Point out every Plasmodium parasite.
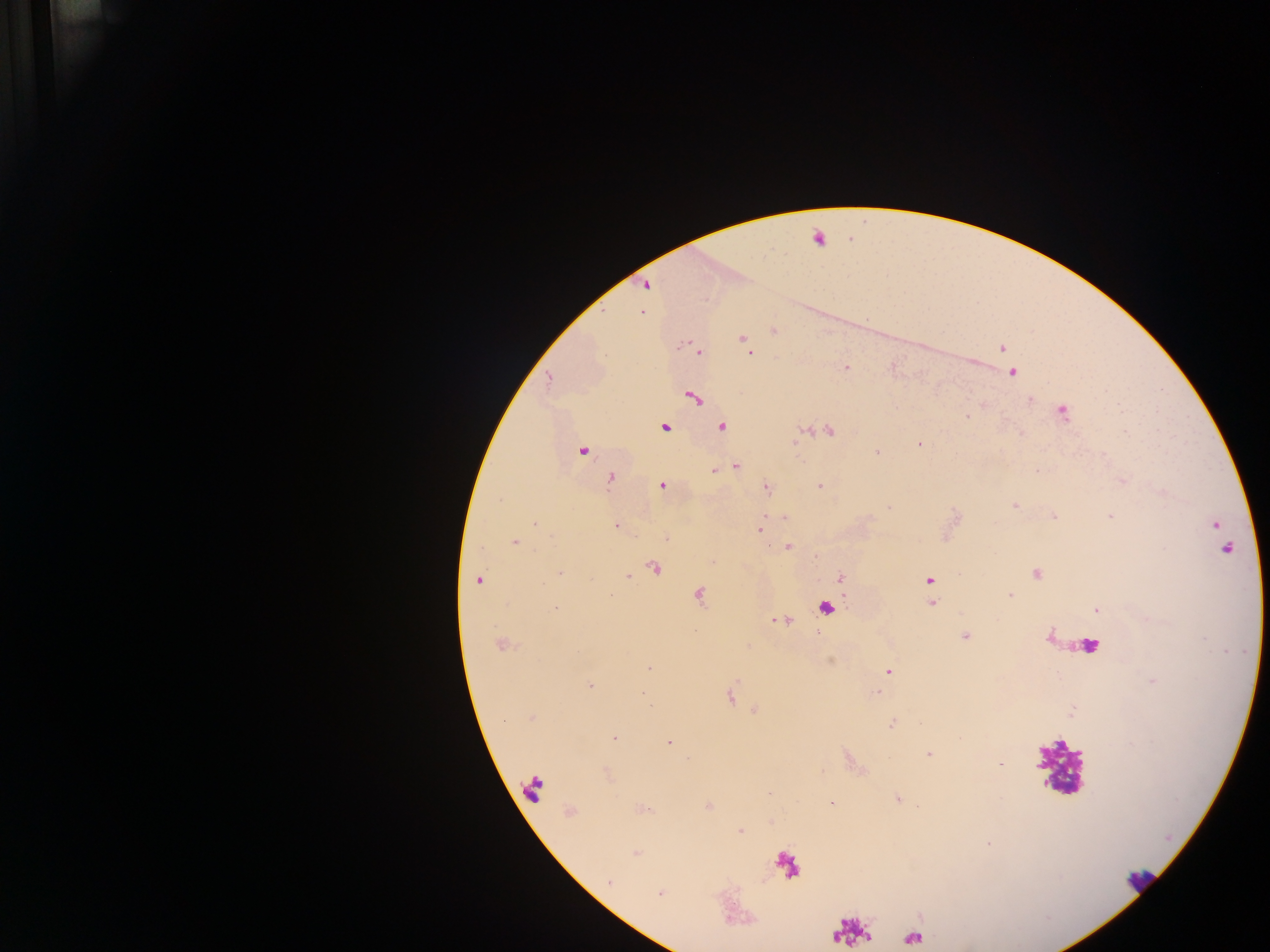

Approximate centers as x y in pixels.
Plasmodium parasites: 646 284; 641 313; 743 338; 1002 348; 700 352; 750 353; 846 368; 1029 399; 1119 407; 965 416; 722 425; 1020 432; 1123 432; 917 443; 582 450; 877 452; 736 466; 713 471; 1036 471; 1121 481; 660 485; 819 485; 766 487; 1162 493; 500 500; 1012 505; 890 506; 1053 515; 1108 515; 783 516; 534 525; 616 526; 1215 526; 758 529; 667 539; 514 542; 787 546; 814 557; 712 560; 560 574; 1036 574; 628 576; 839 579; 480 580; 929 581; 1009 594; 931 603; 558 607; 1097 609; 772 620; 1149 621; 964 636; 647 668; 889 672; 1152 678; 592 686; 878 693; 644 694; 530 718; 504 720; 894 723; 614 737; 671 742; 928 754; 1000 764; 769 794; 897 798; 832 803; 918 804; 740 831; 988 843; 660 895.

image size = 1270×952 pixels
field of view = single
country = Ghana
leukocyte locations = approximate centers as x y in pixels: 1084 653; 1063 768; 534 786; 785 863; 1134 883; 850 932; 909 939
capture = mobile-phone photograph through a microscope
preparation = thick blood smear